Report the malaria status of this cell.
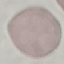
Uninfected.

{
  "image_type": "cell patch, automatically extracted from a larger field of view and resized to 64 × 64 pixels",
  "preparation": "thin blood smear",
  "stain": "Giemsa",
  "capture": "smartphone camera at the microscope eyepiece"
}